Report the malaria status of this cell.
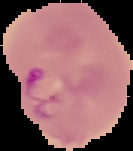
Parasitized.

{
  "image_type": "segmented cell region on a black background",
  "image_size": "133×151 pixels",
  "preparation": "thin blood smear"
}